Locate every Plasmodium ovale-infected red blood cell.
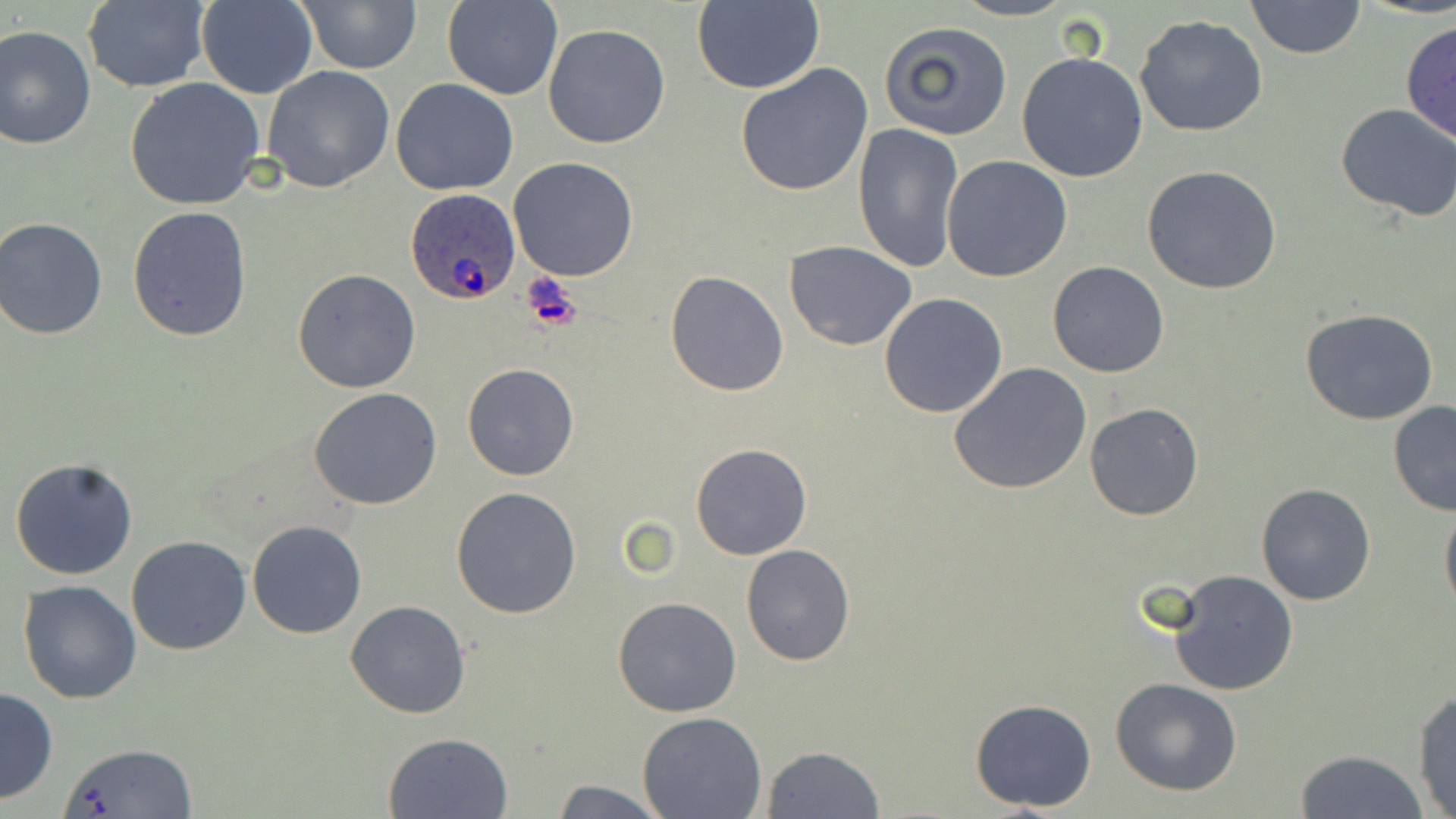
Approximate bounding boxes as (x1, y1, x2, y2) in pixels.
Plasmodium ovale-infected red blood cells: (405, 188, 520, 306).

Uninfected red blood cell locations: (196, 0, 317, 99), (295, 0, 422, 73), (951, 0, 1077, 22), (1244, 0, 1365, 60), (82, 1, 209, 93), (441, 1, 563, 101), (691, 1, 824, 95), (1134, 15, 1268, 138), (880, 19, 1014, 140), (1401, 19, 1456, 147), (542, 23, 671, 149), (0, 25, 96, 150), (1016, 52, 1148, 182), (734, 62, 875, 197), (261, 65, 397, 194), (124, 77, 266, 212), (392, 78, 519, 197), (1335, 103, 1456, 221), (851, 122, 963, 274), (942, 154, 1072, 283), (508, 156, 639, 281), (1141, 165, 1284, 296), (127, 207, 253, 342), (0, 216, 109, 340), (785, 241, 915, 350), (1048, 260, 1169, 378), (292, 268, 421, 392), (665, 271, 789, 396), (878, 293, 1007, 418), (1300, 309, 1440, 425), (949, 362, 1092, 495), (461, 364, 580, 481), (309, 388, 442, 511), (1387, 400, 1456, 517), (1083, 401, 1204, 520), (690, 443, 812, 560), (9, 456, 139, 580), (1256, 483, 1376, 605), (450, 486, 583, 618), (1440, 497, 1456, 618), (247, 520, 366, 638), (126, 536, 252, 656), (740, 544, 854, 667), (1167, 570, 1297, 696), (19, 581, 142, 702), (613, 596, 742, 718), (345, 600, 472, 719), (1110, 678, 1243, 798), (0, 687, 58, 804), (1412, 689, 1455, 817), (970, 697, 1097, 812), (637, 710, 766, 818), (383, 732, 513, 819), (60, 741, 199, 818), (761, 746, 885, 819), (1297, 750, 1428, 819), (546, 780, 667, 818). Slide-level diagnosis: Plasmodium ovale. May-Grünwald-Giemsa stain. Thin blood film. 1000x magnification. Light microscopy. Image is 1456×819 pixels. Single field of view.